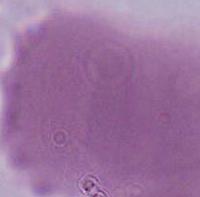
Photomicrograph. Captured at 1000x magnification. A red blood cell is shown.